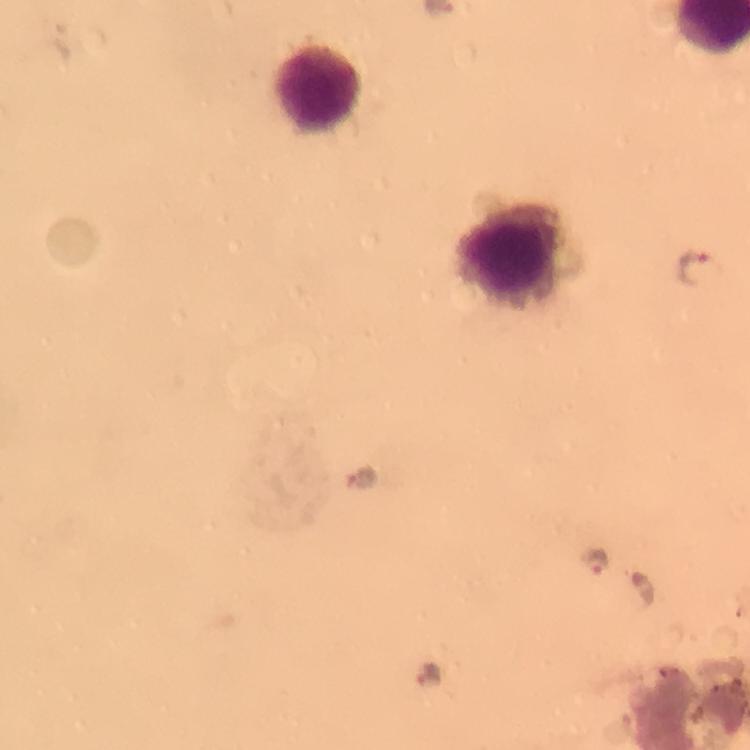

Approximate centers as (x, y) in pixels. Plasmodium parasite locations: (693, 267), (361, 477), (595, 563), (644, 588), (427, 674). Leukocyte locations: (316, 85), (513, 257). Cropped region of a single field of view. Thick blood smear. Giemsa-stained preparation. Image is 750×750 pixels. From a diagnostic examination for malaria. Smartphone photograph taken through a microscope. At 100x magnification. Immersion oil applied.